Give the position of every Plasmodium parasite.
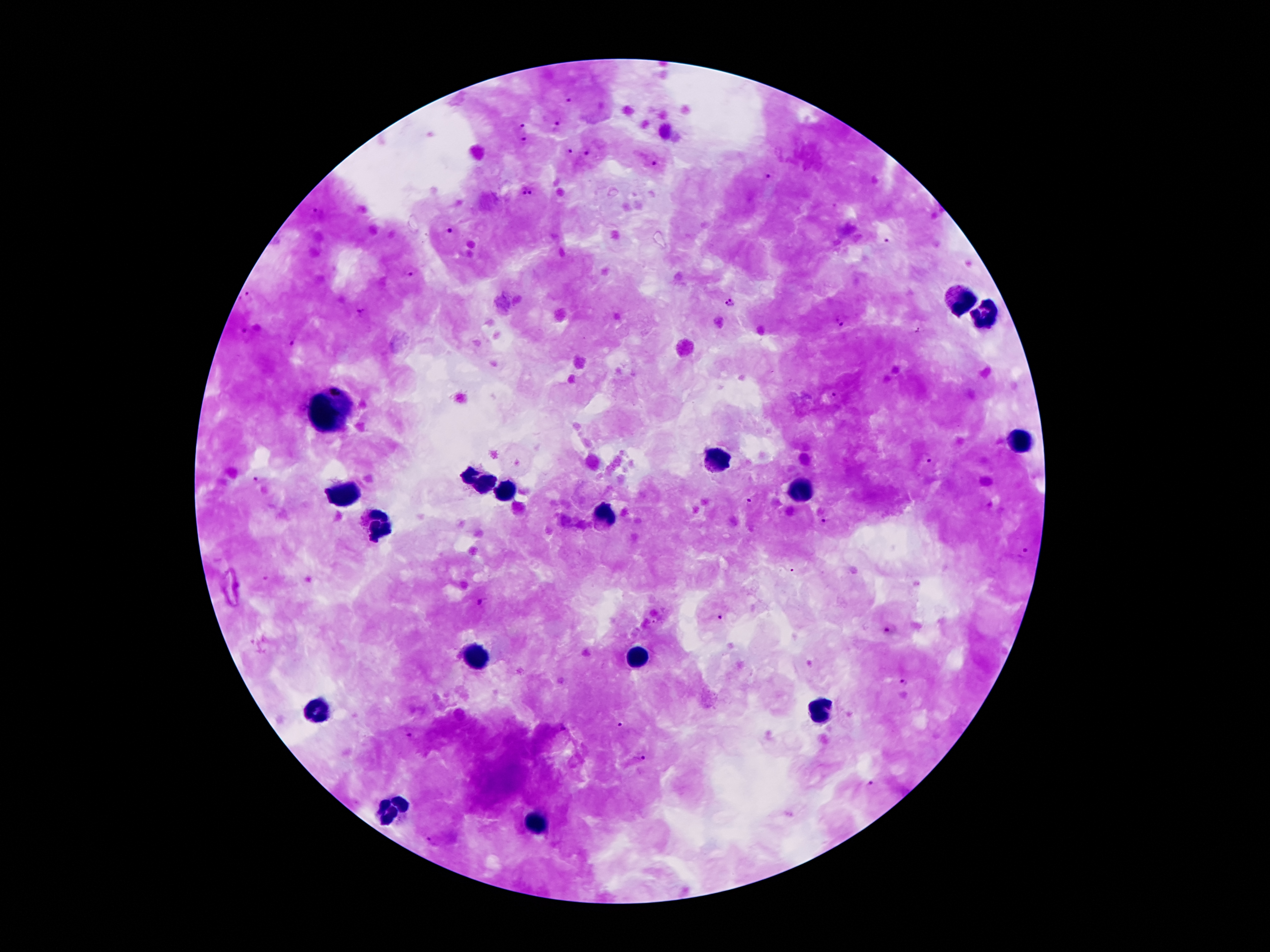

Approximate centers as {x, y} in pixels.
Plasmodium parasites: {569, 97}, {557, 124}, {523, 126}, {524, 140}, {568, 150}, {588, 151}, {652, 159}, {770, 176}, {526, 194}, {449, 232}, {887, 240}, {408, 269}, {246, 298}, {730, 302}, {361, 311}, {840, 320}, {244, 331}, {918, 331}, {296, 339}, {831, 396}, {925, 458}, {256, 480}, {751, 501}, {824, 520}, {1024, 552}, {791, 570}, {484, 601}, {722, 617}, {891, 630}, {904, 683}, {619, 723}, {563, 729}, {409, 736}, {639, 758}, {872, 785}, {432, 840}.

Summary:
  - Leukocyte locations: {957, 300}, {984, 316}, {328, 414}, {1016, 437}, {718, 459}, {479, 481}, {505, 491}, {350, 493}, {800, 493}, {603, 514}, {378, 521}, {639, 654}, {475, 656}, {319, 709}, {821, 709}, {391, 809}, {534, 822}
  - Stain: Giemsa
  - Image size: 1270×952 pixels
  - Patient malaria status: infected with Plasmodium falciparum
  - Capture: smartphone camera through the microscope eyepiece
  - Magnification: 100x
  - Preparation: thick blood smear
  - Field of view: one from this slide